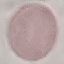 Result: no malaria parasites seen. Automatically extracted cell patch, resized to 64 × 64 pixels. Giemsa-stained preparation. Thin blood smear. Photographed with a smartphone camera at the microscope eyepiece.